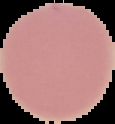

result: negative for malaria parasites
image_size: 115×124 pixels
preparation: thin blood film
image_type: segmented cell region on a black background